Assess this cell for malaria.
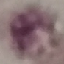

It is uninfected.

stain = Giemsa
preparation = thin blood smear
capture = smartphone through the microscope eyepiece
image type = cell patch, automatically extracted from a larger field of view and resized to 64 × 64 pixels